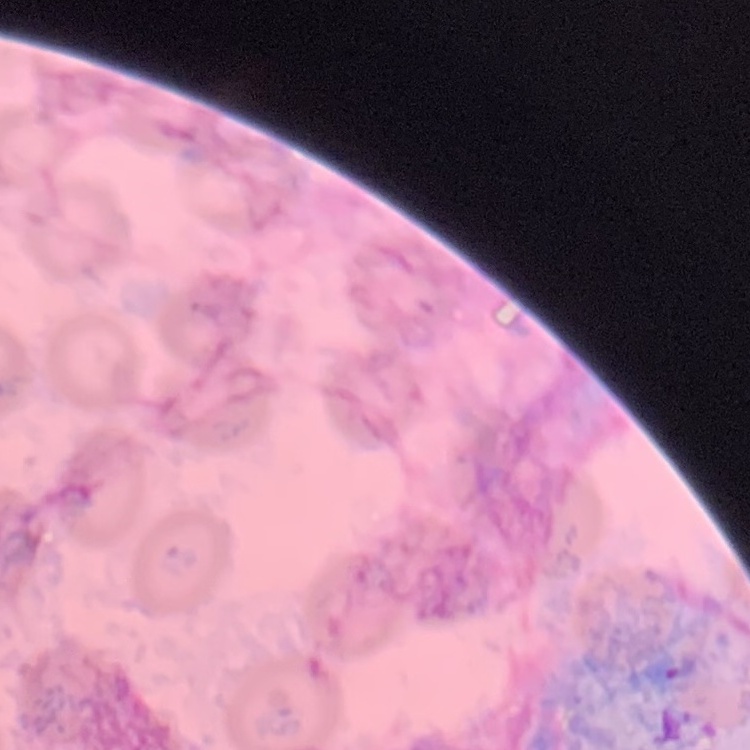
erythrocyte morphology = no rouleaux formation
stain = Field's or Giemsa
image type = square crop of a larger photomicrograph
preparation = thin blood smear